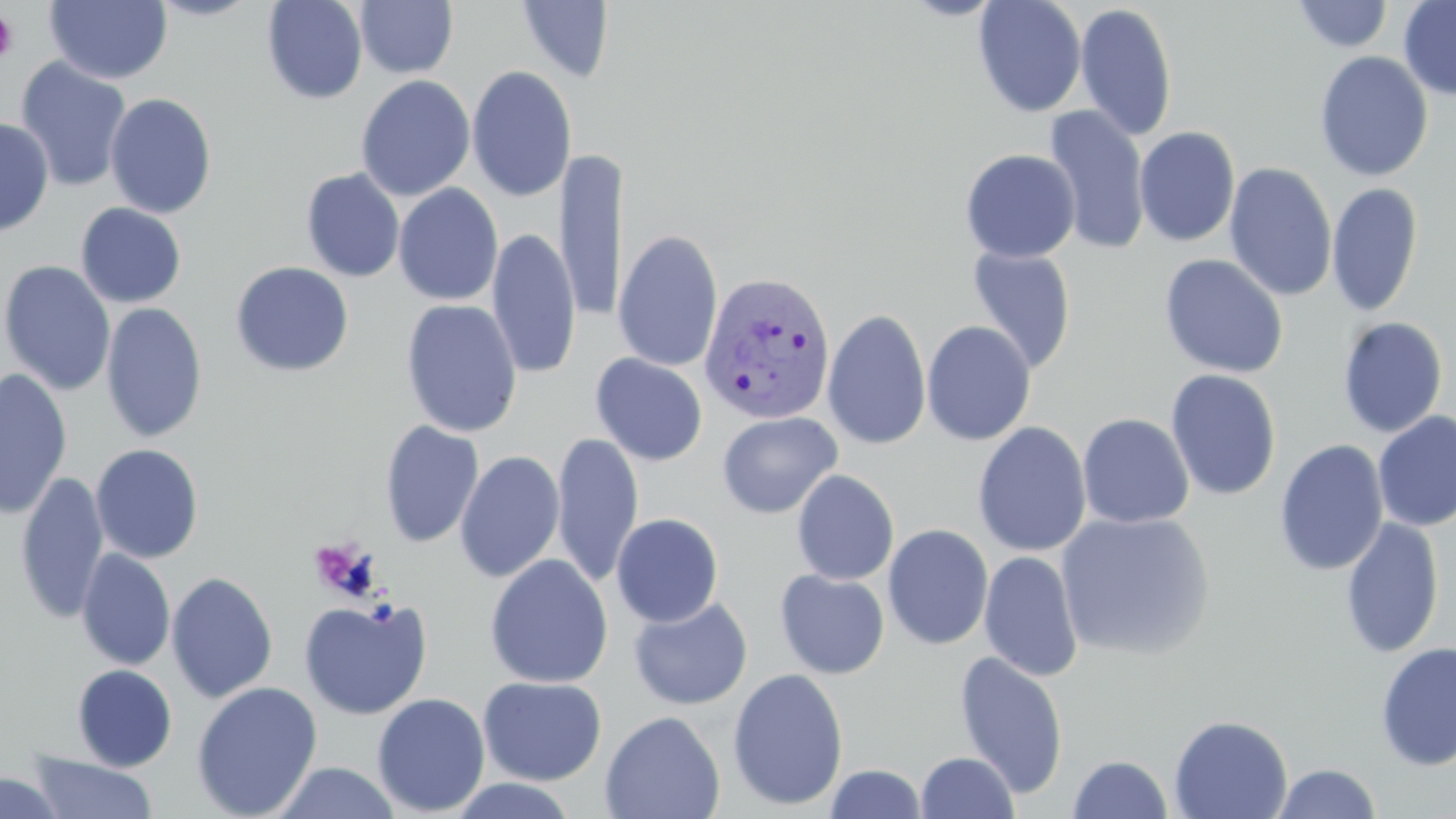
Summary:
  - Coordinate format: approximate bounding boxes as (x1,y1)-(x2,y2) corner pairs in pixels
  - Plasmodium vivax-infected red blood cell locations: (697,272)-(836,426)
  - Platelet locations: (0,11)-(18,62)
  - Uninfected red blood cell locations: (45,0)-(172,84), (145,0)-(265,21), (261,0)-(368,105), (355,0)-(458,79), (972,0)-(1087,117), (1398,0)-(1456,101), (516,1)-(615,84), (1292,1)-(1393,53), (1075,3)-(1177,142), (1314,50)-(1434,182), (14,57)-(133,192), (466,65)-(577,202), (356,75)-(475,201), (105,93)-(217,219), (1042,105)-(1151,255), (0,117)-(54,237), (1134,126)-(1240,247), (557,147)-(627,324), (960,149)-(1081,263), (1224,162)-(1337,302), (301,169)-(405,282), (1327,182)-(1423,318), (393,184)-(503,306), (75,203)-(187,307), (488,227)-(580,379), (613,230)-(723,373), (965,246)-(1077,375), (1158,254)-(1289,378), (1,260)-(116,396), (230,261)-(354,377), (401,299)-(522,437), (100,302)-(208,443), (823,307)-(932,451), (1337,316)-(1448,438), (921,320)-(1036,446), (590,353)-(708,466), (0,368)-(73,520), (1165,369)-(1282,500), (717,411)-(842,519), (1373,411)-(1456,532), (1077,413)-(1194,529), (378,420)-(484,548), (972,421)-(1092,557), (551,432)-(643,588), (1274,439)-(1389,576), (90,443)-(204,564), (455,450)-(565,583), (791,469)-(899,585), (15,470)-(109,625), (1055,510)-(1215,661), (611,513)-(724,628), (1340,516)-(1445,658), (883,523)-(994,651), (76,548)-(175,671), (979,551)-(1085,681), (484,553)-(613,689), (774,569)-(890,679), (167,571)-(279,704), (628,596)-(753,710), (299,597)-(432,719), (1375,641)-(1456,771), (954,650)-(1069,798), (72,664)-(177,771), (727,668)-(849,811), (478,676)-(607,786), (191,681)-(323,818), (372,693)-(490,816), (600,710)-(725,819), (1168,714)-(1293,819), (28,751)-(158,818), (916,751)-(1019,818), (1067,754)-(1173,818), (271,761)-(403,818), (1272,763)-(1382,818), (824,764)-(928,819), (0,772)-(69,819), (445,778)-(580,818)
  - Slide-level diagnosis: Plasmodium vivax
  - Modality: optical microscopy
  - Stain: May-Grünwald-Giemsa
  - Preparation: thin blood smear
  - Image size: 1456×819 pixels
  - Field of view: single
  - Magnification: 1000x